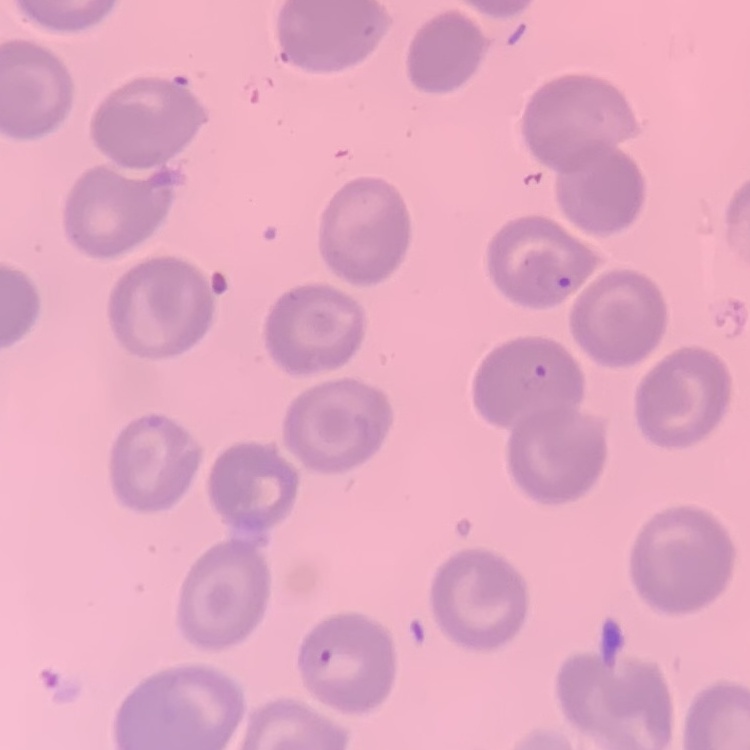
Summary:
  - Red blood cell morphology: no rouleaux formation
  - Stain: Field's or Giemsa
  - Preparation: thin blood smear
  - Image type: one tile cut from a larger photomicrograph